Locate and identify every blood parasite.
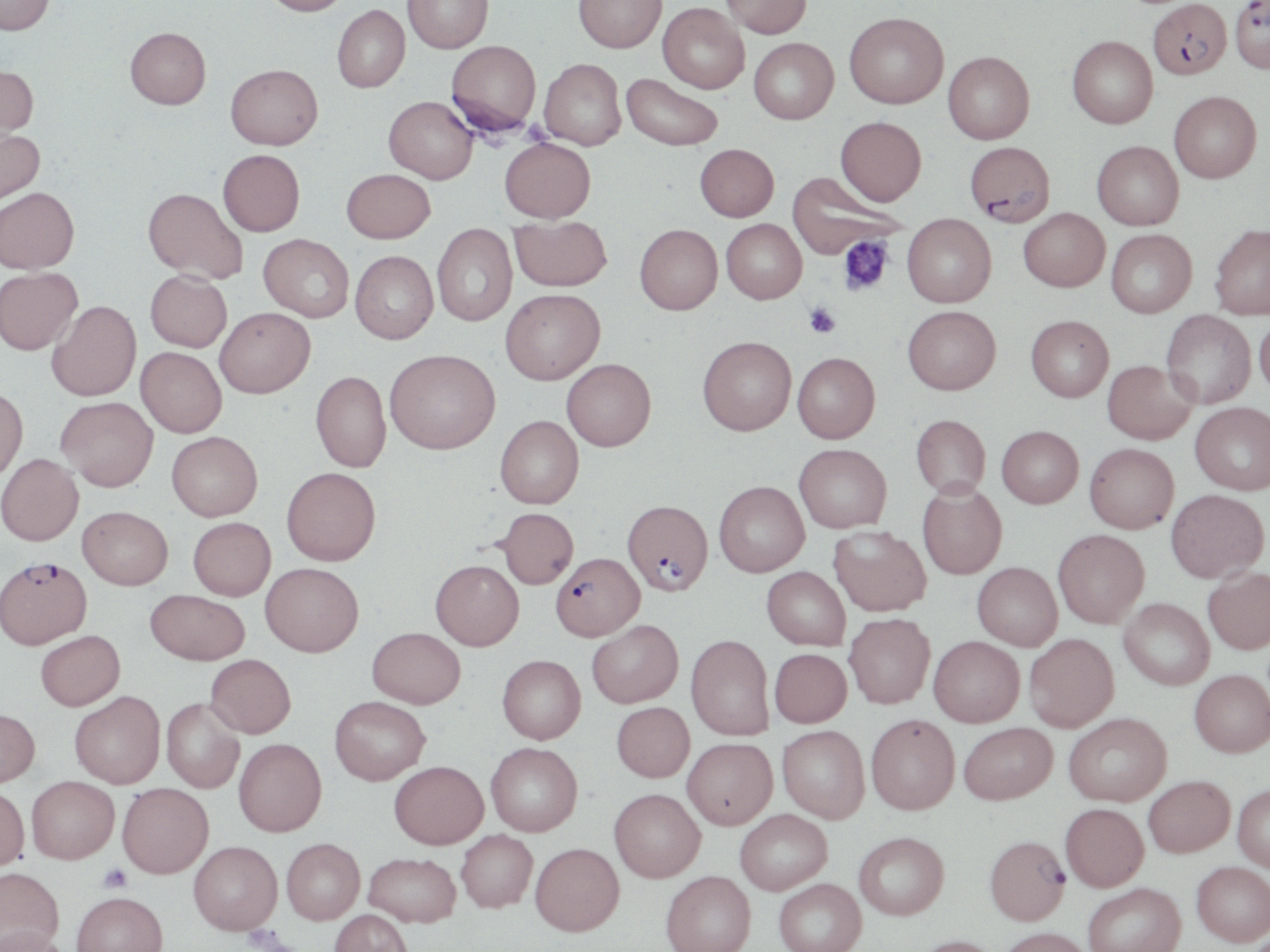

Approximate bounding boxes as named x1/y1/x2/y2 corners in pixels.
Plasmodium falciparum-infected red blood cells: (x1=1230, y1=0, x2=1270, y2=74), (x1=1147, y1=1, x2=1232, y2=80), (x1=965, y1=141, x2=1055, y2=226), (x1=622, y1=498, x2=713, y2=595), (x1=551, y1=552, x2=644, y2=641), (x1=0, y1=555, x2=91, y2=648), (x1=984, y1=834, x2=1070, y2=924).
No Plasmodium ovale, Plasmodium malariae, Plasmodium vivax, Babesia divergens, or Trypanosoma brucei observed.

slide-level diagnosis = Plasmodium falciparum
field of view = one of a larger specimen
image size = 1270×952 pixels
magnification = 1000x
modality = light microscopy
platelet locations = approximate bounding boxes as named x1/y1/x2/y2 corners in pixels: (x1=838, y1=235, x2=893, y2=296), (x1=804, y1=303, x2=840, y2=338), (x1=97, y1=863, x2=132, y2=892)
uninfected red blood cell locations = approximate bounding boxes as named x1/y1/x2/y2 corners in pixels: (x1=1, y1=0, x2=55, y2=35), (x1=261, y1=0, x2=353, y2=16), (x1=403, y1=0, x2=493, y2=53), (x1=574, y1=0, x2=667, y2=53), (x1=721, y1=0, x2=812, y2=38), (x1=657, y1=3, x2=749, y2=94), (x1=332, y1=5, x2=410, y2=92), (x1=844, y1=12, x2=949, y2=109), (x1=125, y1=27, x2=211, y2=109), (x1=1067, y1=35, x2=1158, y2=128), (x1=749, y1=37, x2=839, y2=124), (x1=446, y1=40, x2=542, y2=137), (x1=943, y1=51, x2=1035, y2=144), (x1=539, y1=58, x2=627, y2=150), (x1=225, y1=63, x2=323, y2=149), (x1=0, y1=65, x2=38, y2=143), (x1=621, y1=73, x2=723, y2=151), (x1=1169, y1=91, x2=1261, y2=183), (x1=384, y1=96, x2=478, y2=184), (x1=835, y1=116, x2=926, y2=206), (x1=0, y1=127, x2=44, y2=205), (x1=500, y1=138, x2=595, y2=222), (x1=1092, y1=141, x2=1183, y2=230), (x1=695, y1=143, x2=779, y2=221), (x1=218, y1=149, x2=305, y2=236), (x1=342, y1=168, x2=435, y2=243), (x1=787, y1=171, x2=906, y2=259), (x1=0, y1=187, x2=79, y2=273), (x1=143, y1=187, x2=247, y2=284), (x1=1018, y1=207, x2=1110, y2=291), (x1=902, y1=213, x2=997, y2=307), (x1=509, y1=215, x2=611, y2=291), (x1=721, y1=219, x2=807, y2=304), (x1=432, y1=223, x2=517, y2=326), (x1=1209, y1=223, x2=1270, y2=319), (x1=635, y1=224, x2=722, y2=314), (x1=1106, y1=229, x2=1197, y2=317), (x1=259, y1=233, x2=354, y2=322), (x1=350, y1=250, x2=438, y2=343), (x1=0, y1=267, x2=82, y2=354), (x1=145, y1=270, x2=232, y2=352), (x1=500, y1=288, x2=605, y2=384), (x1=47, y1=300, x2=141, y2=401), (x1=902, y1=305, x2=1001, y2=394), (x1=214, y1=307, x2=315, y2=398), (x1=1160, y1=310, x2=1256, y2=409), (x1=1254, y1=314, x2=1270, y2=399), (x1=1026, y1=315, x2=1114, y2=402), (x1=697, y1=336, x2=796, y2=435), (x1=136, y1=347, x2=226, y2=437), (x1=385, y1=348, x2=500, y2=454), (x1=792, y1=352, x2=880, y2=443), (x1=562, y1=358, x2=656, y2=451), (x1=1102, y1=359, x2=1197, y2=444), (x1=311, y1=370, x2=391, y2=472), (x1=0, y1=386, x2=28, y2=483), (x1=55, y1=396, x2=158, y2=491), (x1=1190, y1=402, x2=1270, y2=494), (x1=911, y1=414, x2=991, y2=497), (x1=495, y1=415, x2=583, y2=508), (x1=997, y1=425, x2=1083, y2=508), (x1=167, y1=431, x2=262, y2=521), (x1=794, y1=443, x2=892, y2=532), (x1=1084, y1=443, x2=1179, y2=533), (x1=0, y1=453, x2=83, y2=545), (x1=282, y1=467, x2=380, y2=565), (x1=714, y1=481, x2=810, y2=576), (x1=917, y1=481, x2=1007, y2=579), (x1=1165, y1=488, x2=1268, y2=582), (x1=77, y1=506, x2=173, y2=589), (x1=497, y1=508, x2=578, y2=588), (x1=188, y1=517, x2=275, y2=600), (x1=829, y1=525, x2=931, y2=616), (x1=1053, y1=529, x2=1149, y2=627), (x1=430, y1=559, x2=524, y2=650), (x1=261, y1=562, x2=364, y2=656), (x1=972, y1=562, x2=1062, y2=650), (x1=761, y1=566, x2=850, y2=650), (x1=1203, y1=566, x2=1270, y2=654), (x1=145, y1=589, x2=250, y2=665), (x1=1119, y1=597, x2=1214, y2=690), (x1=844, y1=612, x2=935, y2=708), (x1=587, y1=619, x2=683, y2=707), (x1=368, y1=627, x2=466, y2=708), (x1=36, y1=630, x2=125, y2=710), (x1=1024, y1=633, x2=1119, y2=731), (x1=686, y1=634, x2=774, y2=740), (x1=929, y1=635, x2=1025, y2=727), (x1=769, y1=648, x2=852, y2=727), (x1=205, y1=654, x2=296, y2=738), (x1=498, y1=654, x2=586, y2=743), (x1=1190, y1=669, x2=1270, y2=756), (x1=70, y1=691, x2=165, y2=788), (x1=330, y1=696, x2=430, y2=784), (x1=161, y1=697, x2=244, y2=793), (x1=612, y1=701, x2=695, y2=782), (x1=0, y1=707, x2=40, y2=787), (x1=1064, y1=712, x2=1171, y2=806), (x1=866, y1=713, x2=960, y2=814), (x1=958, y1=722, x2=1057, y2=804), (x1=777, y1=725, x2=870, y2=823), (x1=682, y1=737, x2=778, y2=828), (x1=234, y1=738, x2=327, y2=836), (x1=486, y1=742, x2=582, y2=836), (x1=389, y1=760, x2=488, y2=849), (x1=27, y1=775, x2=119, y2=863), (x1=1144, y1=775, x2=1234, y2=857), (x1=117, y1=782, x2=213, y2=878), (x1=1233, y1=784, x2=1270, y2=871), (x1=0, y1=785, x2=29, y2=871), (x1=609, y1=788, x2=705, y2=881), (x1=1060, y1=803, x2=1149, y2=891), (x1=735, y1=809, x2=832, y2=894), (x1=456, y1=829, x2=537, y2=912), (x1=854, y1=831, x2=949, y2=920), (x1=282, y1=837, x2=365, y2=923), (x1=188, y1=840, x2=282, y2=934), (x1=530, y1=842, x2=624, y2=935), (x1=363, y1=852, x2=460, y2=927), (x1=1191, y1=861, x2=1270, y2=946), (x1=0, y1=866, x2=64, y2=950), (x1=660, y1=870, x2=756, y2=952), (x1=773, y1=878, x2=866, y2=952), (x1=1083, y1=882, x2=1185, y2=952), (x1=72, y1=891, x2=168, y2=952), (x1=329, y1=909, x2=413, y2=952), (x1=997, y1=927, x2=1093, y2=952), (x1=0, y1=928, x2=74, y2=952), (x1=912, y1=935, x2=1005, y2=952)
preparation = thin blood film
stain = May-Grünwald-Giemsa